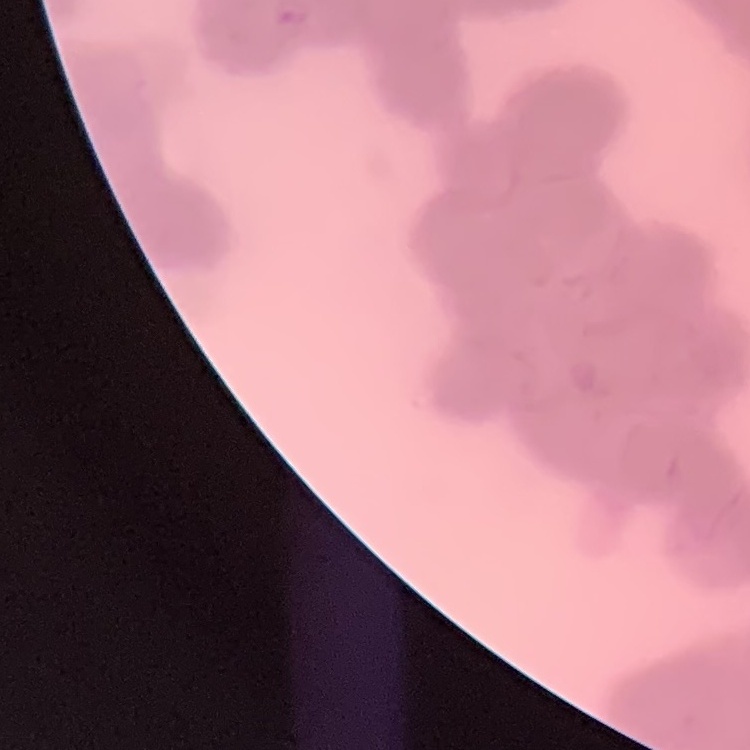
Summary:
  - Red blood cell morphology: rouleaux formation
  - Preparation: thin peripheral smear
  - Image type: one tile cut from a larger photomicrograph
  - Stain: Field's or Giemsa